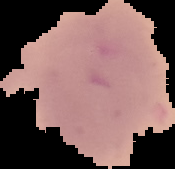
Image is 175×169 pixels. Cell region segmented out of the field of view; the surrounding area is masked to black. Result: negative for malaria parasites. From a thin blood film.